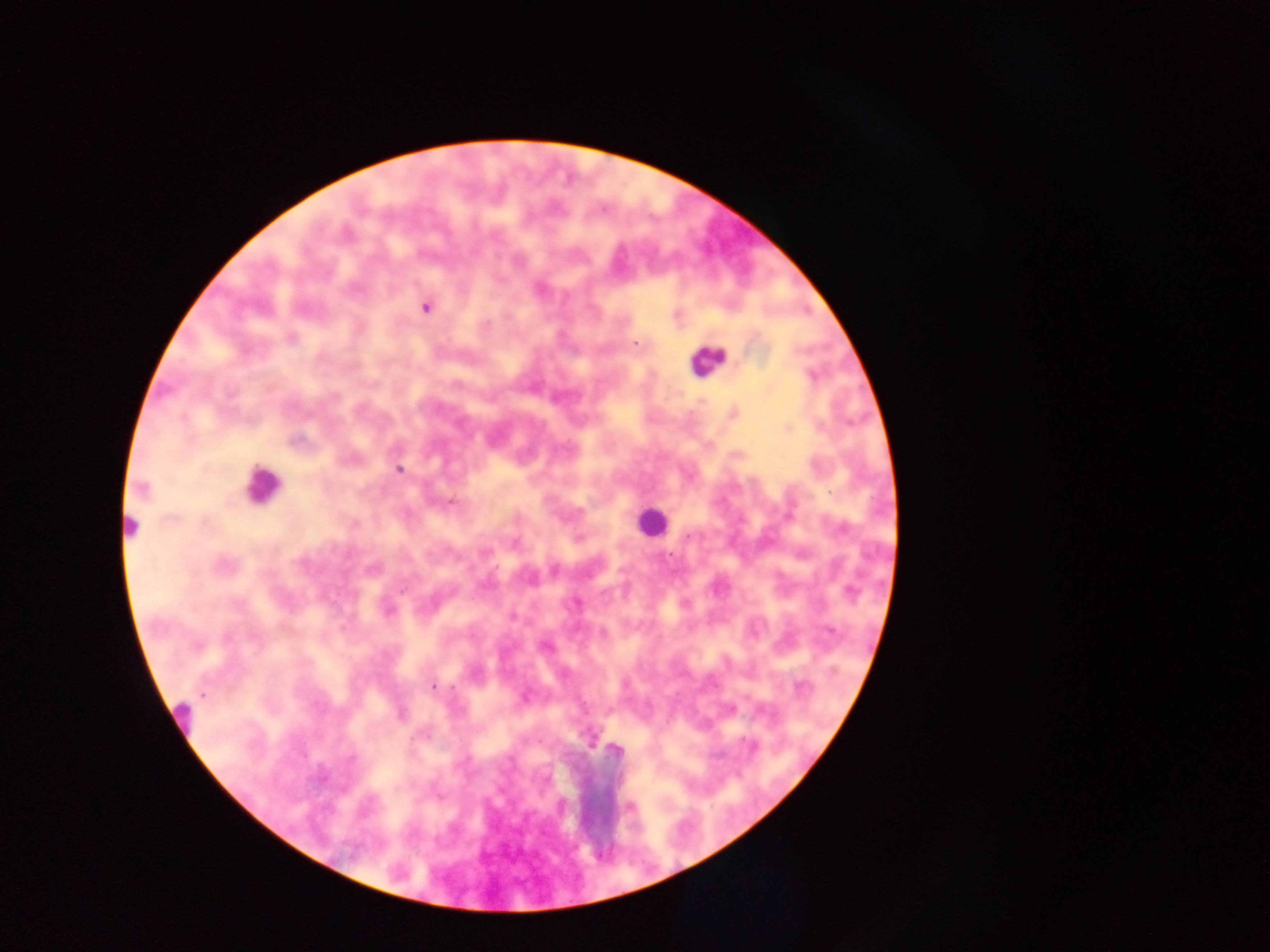
Approximate centers as (x, y) in pixels.
Summary:
  - Plasmodium parasite locations: (425, 308), (290, 339), (636, 342), (812, 375), (335, 397), (788, 429), (297, 440), (399, 469), (142, 489), (452, 502), (355, 523), (688, 537), (514, 542), (223, 565), (554, 570), (402, 590), (685, 604), (388, 611), (255, 638), (197, 646), (545, 646), (433, 687), (800, 687), (401, 714), (615, 750)
  - Leukocyte locations: (707, 360), (261, 484), (647, 521), (131, 524), (178, 721)
  - Preparation: thick blood film
  - Field of view: single
  - Country: Ghana
  - Capture: mobile-phone photograph through a microscope
  - Image size: 1270×952 pixels